Identify the blood parasite species.
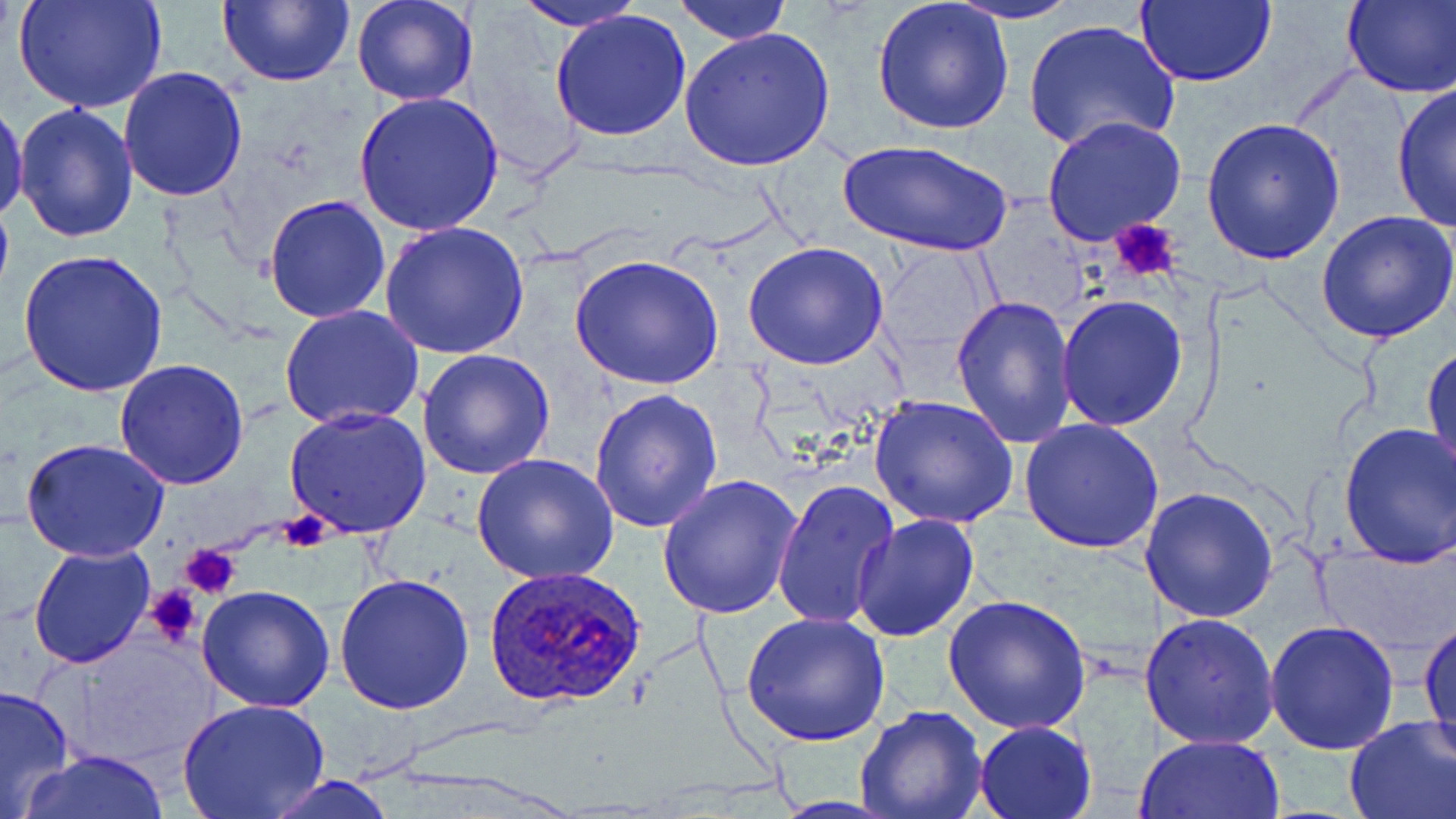
Plasmodium ovale.

platelet locations = approximate bounding boxes as named x1/y1/x2/y2 corners in pixels: (x1=1109, y1=220, x2=1183, y2=284), (x1=271, y1=514, x2=335, y2=550), (x1=181, y1=543, x2=242, y2=598), (x1=144, y1=585, x2=205, y2=646)
image size = 1456×819 pixels
Plasmodium ovale-infected red blood cell locations = approximate bounding boxes as named x1/y1/x2/y2 corners in pixels: (x1=485, y1=566, x2=648, y2=708)
preparation = thin blood smear
field of view = one of a larger specimen
stain = May-Grünwald-Giemsa
magnification = 1000x
modality = optical microscopy
uninfected red blood cell locations = approximate bounding boxes as named x1/y1/x2/y2 corners in pixels: (x1=10, y1=0, x2=170, y2=115), (x1=217, y1=0, x2=353, y2=87), (x1=350, y1=0, x2=478, y2=106), (x1=673, y1=0, x2=792, y2=44), (x1=943, y1=0, x2=1084, y2=24), (x1=1135, y1=0, x2=1279, y2=88), (x1=1342, y1=0, x2=1456, y2=99), (x1=518, y1=2, x2=645, y2=32), (x1=873, y1=2, x2=1013, y2=136), (x1=549, y1=9, x2=694, y2=142), (x1=1023, y1=20, x2=1179, y2=155), (x1=678, y1=26, x2=836, y2=171), (x1=117, y1=66, x2=249, y2=202), (x1=1390, y1=83, x2=1456, y2=234), (x1=352, y1=91, x2=503, y2=237), (x1=0, y1=101, x2=27, y2=227), (x1=14, y1=102, x2=138, y2=244), (x1=1040, y1=114, x2=1188, y2=246), (x1=1201, y1=118, x2=1347, y2=266), (x1=838, y1=138, x2=1013, y2=258), (x1=262, y1=194, x2=392, y2=323), (x1=1316, y1=211, x2=1456, y2=343), (x1=379, y1=220, x2=530, y2=360), (x1=744, y1=241, x2=888, y2=372), (x1=875, y1=246, x2=999, y2=366), (x1=21, y1=250, x2=167, y2=397), (x1=568, y1=255, x2=725, y2=392), (x1=951, y1=294, x2=1078, y2=447), (x1=1056, y1=296, x2=1188, y2=432), (x1=280, y1=305, x2=425, y2=430), (x1=1424, y1=345, x2=1455, y2=480), (x1=417, y1=349, x2=555, y2=480), (x1=113, y1=358, x2=249, y2=489), (x1=589, y1=385, x2=723, y2=533), (x1=868, y1=394, x2=1019, y2=529), (x1=285, y1=406, x2=431, y2=540), (x1=1020, y1=417, x2=1167, y2=555), (x1=1335, y1=421, x2=1456, y2=567), (x1=20, y1=438, x2=170, y2=562), (x1=472, y1=452, x2=619, y2=584), (x1=658, y1=474, x2=802, y2=619), (x1=772, y1=476, x2=900, y2=632), (x1=1138, y1=487, x2=1280, y2=623), (x1=853, y1=515, x2=980, y2=643), (x1=29, y1=541, x2=158, y2=668), (x1=1314, y1=545, x2=1451, y2=658), (x1=333, y1=572, x2=476, y2=714), (x1=196, y1=586, x2=336, y2=713), (x1=943, y1=594, x2=1092, y2=734), (x1=740, y1=610, x2=891, y2=746), (x1=1139, y1=612, x2=1280, y2=749), (x1=1419, y1=616, x2=1456, y2=767), (x1=1266, y1=619, x2=1401, y2=755), (x1=0, y1=685, x2=74, y2=817), (x1=178, y1=698, x2=330, y2=819), (x1=855, y1=703, x2=988, y2=819), (x1=1342, y1=716, x2=1456, y2=819), (x1=973, y1=720, x2=1097, y2=818), (x1=1134, y1=732, x2=1285, y2=818), (x1=23, y1=749, x2=169, y2=819), (x1=257, y1=775, x2=402, y2=818)